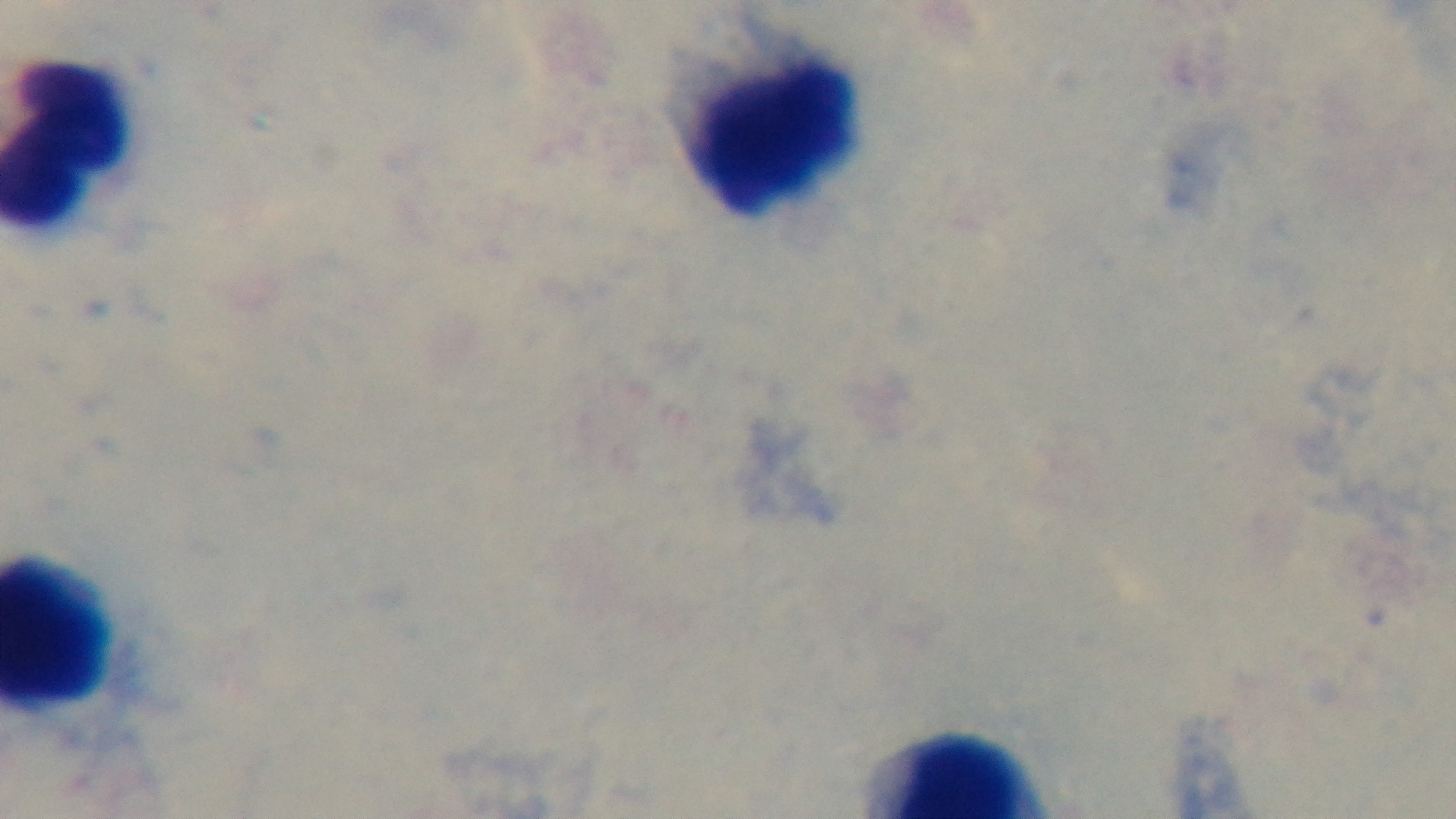

field of view = single
malaria status = uninfected
objective = 100x oil immersion
modality = light microscopy
preparation = thick
capture = mounted 4K digital camera
stain = Giemsa